Classify this cell by malaria status.
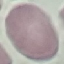
It is uninfected.

Summary:
  - Capture: smartphone through the microscope eyepiece
  - Image type: cell patch, automatically extracted from a larger field of view and resized to 64 × 64 pixels
  - Preparation: thin blood film
  - Stain: Giemsa